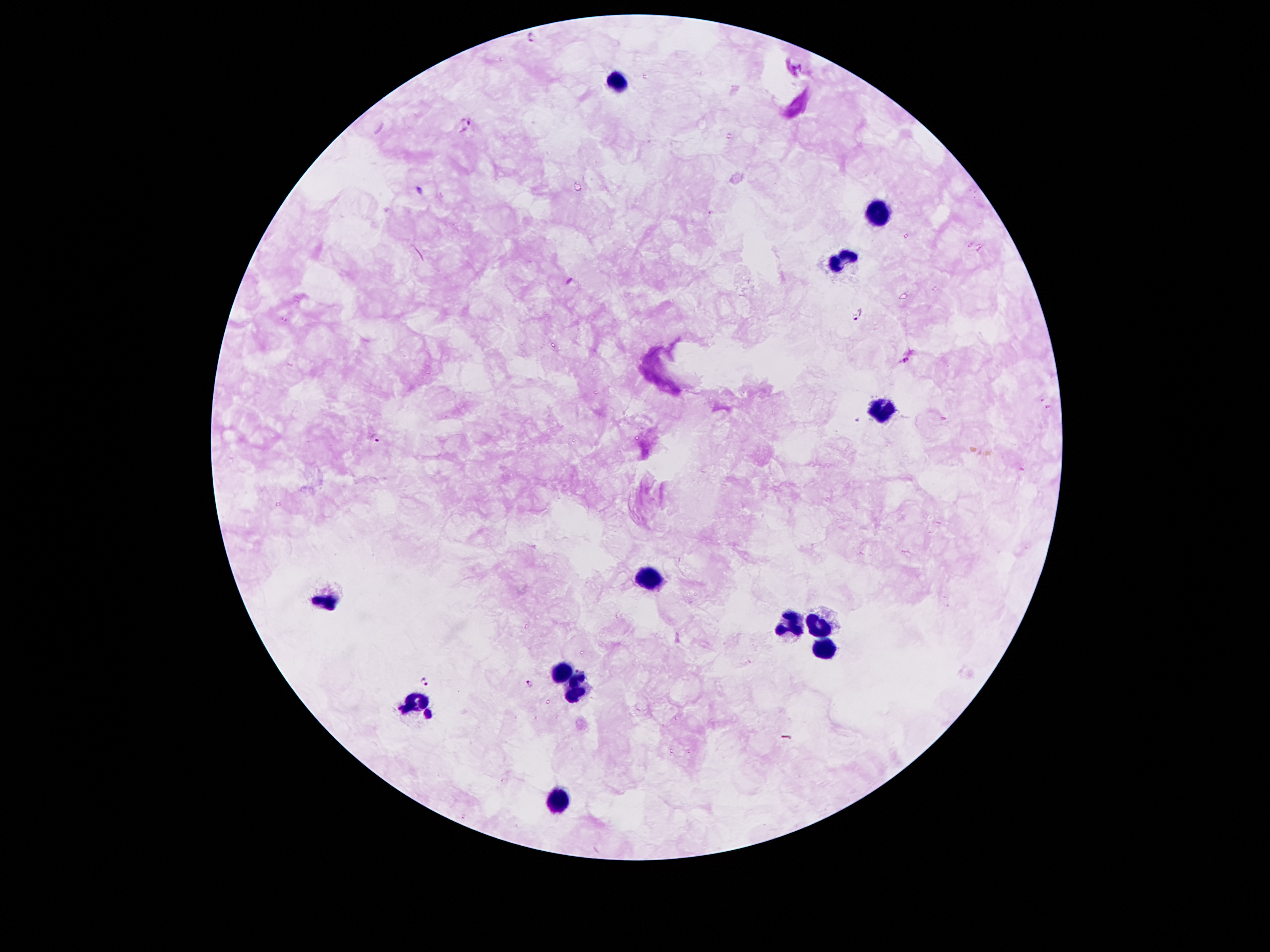
Approximate centers as [x, y] in pixels. Malaria parasite locations: [533, 37], [466, 122], [858, 316], [908, 361], [378, 436], [425, 682], [531, 684]. Leukocyte locations: [619, 80], [880, 211], [842, 261], [882, 409], [650, 573], [329, 603], [787, 622], [820, 622], [827, 652], [561, 669], [577, 687], [418, 699], [555, 803]. Single field of view. Thick blood smear. Giemsa-stained preparation. Image is 1270×952 pixels. 100x magnification. Photographed through the microscope eyepiece with a smartphone camera. Patient malaria status: infected with Plasmodium falciparum.